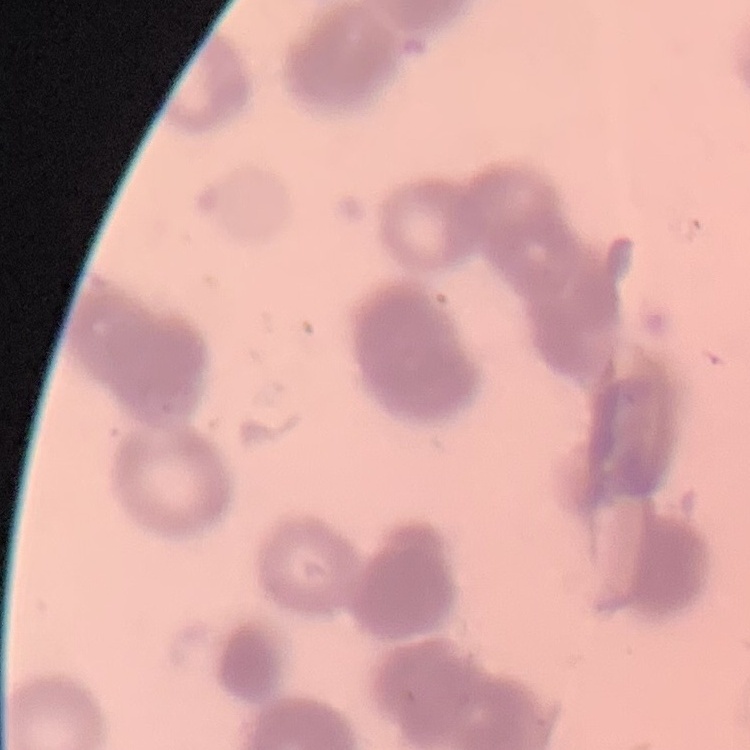
erythrocyte morphology = rouleaux formation
image type = one tile cut from a larger photomicrograph
stain = Field's or Giemsa
preparation = thin blood smear